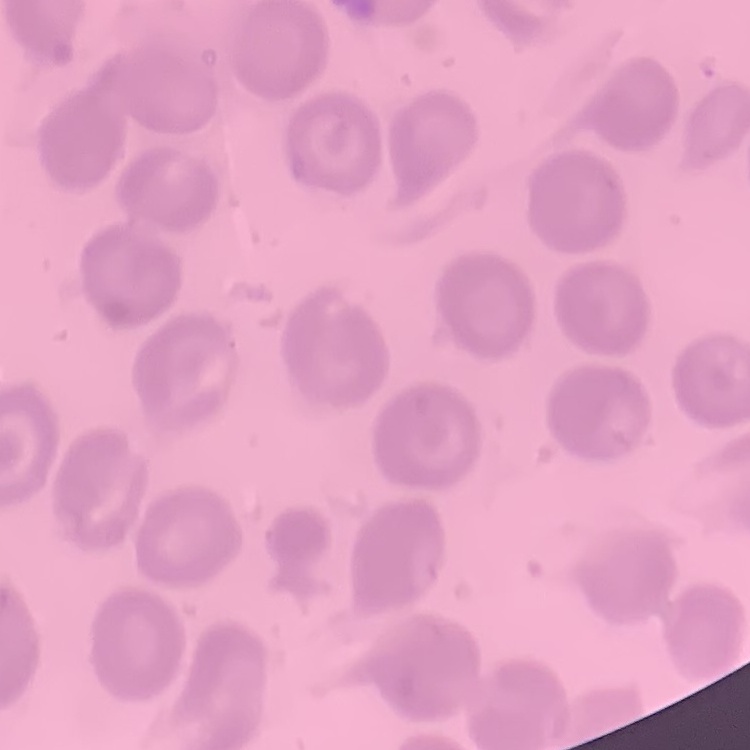
Summary:
  - Red blood cell morphology: no rouleaux formation
  - Image type: square crop of a larger photomicrograph
  - Preparation: thin peripheral smear
  - Stain: Field's or Giemsa